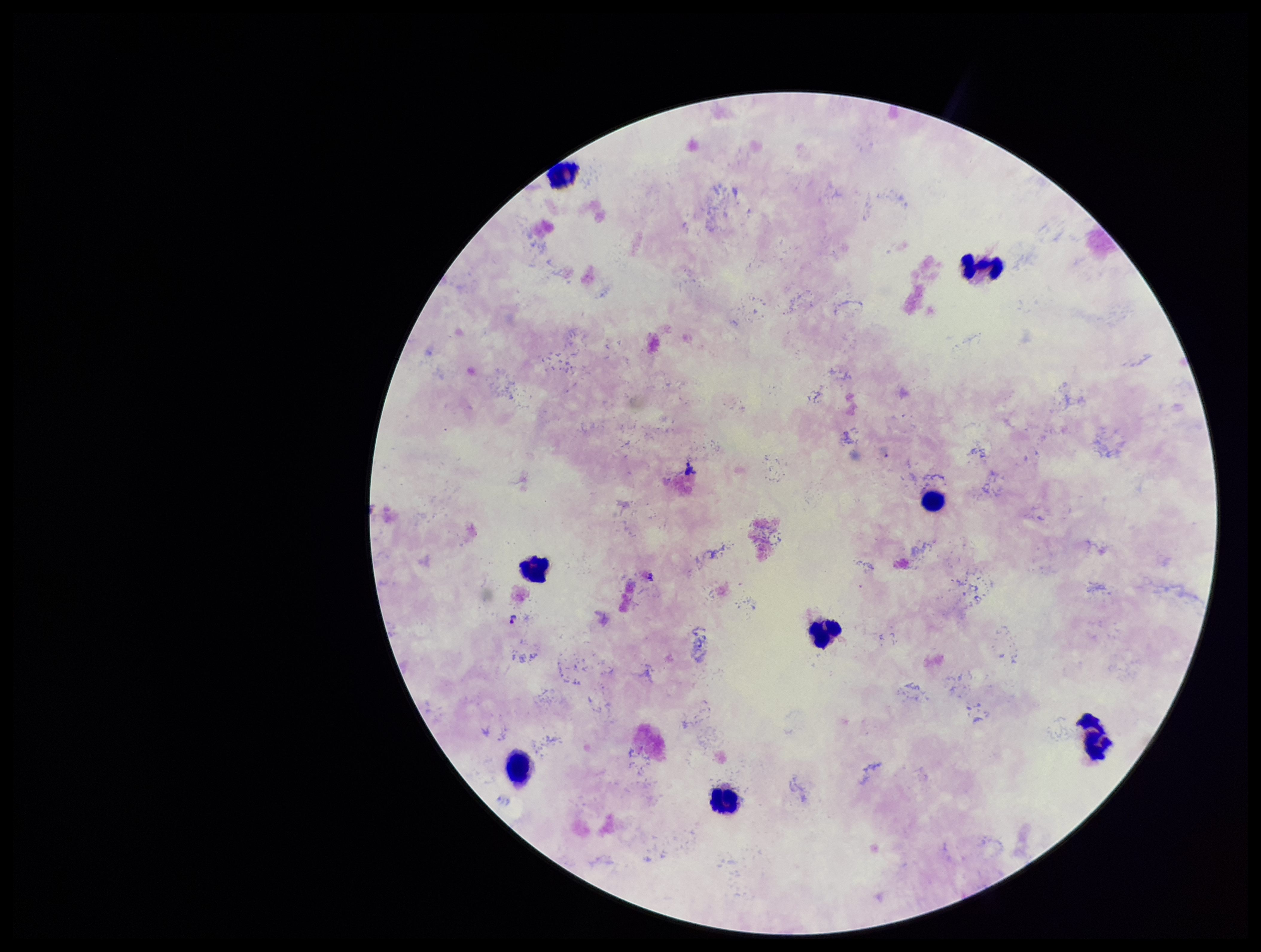
{
  "species_reported_for_this_patient": "Plasmodium falciparum",
  "stain": "Giemsa",
  "patient_malaria_status": "positive",
  "preparation": "thick smear",
  "capture": "smartphone photograph through the microscope eyepiece",
  "field_of_view": "one from this slide",
  "leukocyte_count": 8,
  "plasmodium_parasites": "detected",
  "parasite_count": 1,
  "image_size": "1261×952 pixels"
}